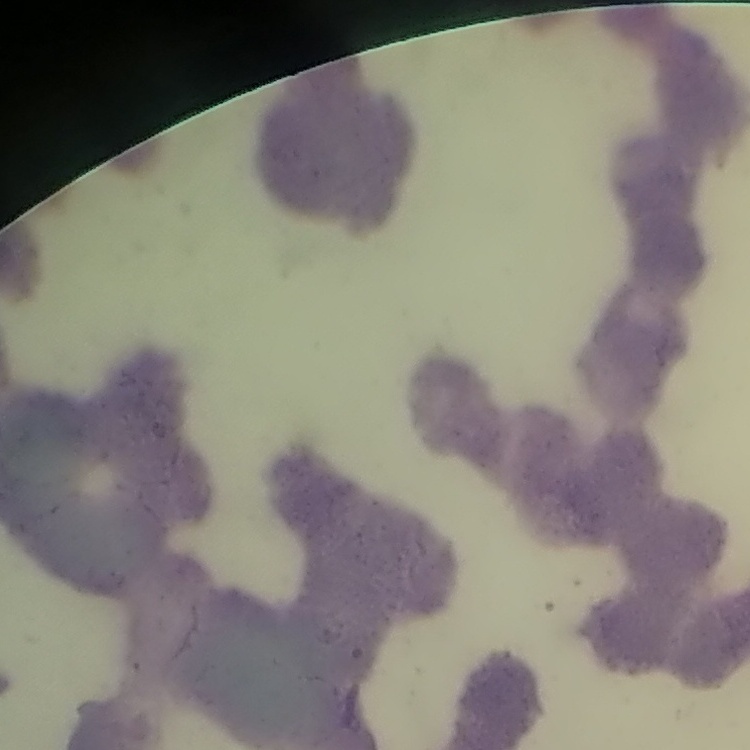

Summary:
  - Red blood cell morphology: rouleaux formation
  - Image type: square crop of a larger photomicrograph
  - Stain: Field's or Giemsa
  - Preparation: thin blood film